State which parasite is depicted.
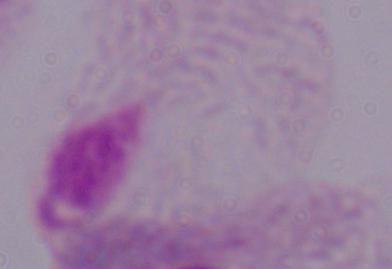
This is a trichomonad.

modality = photomicrograph
magnification = 1000x